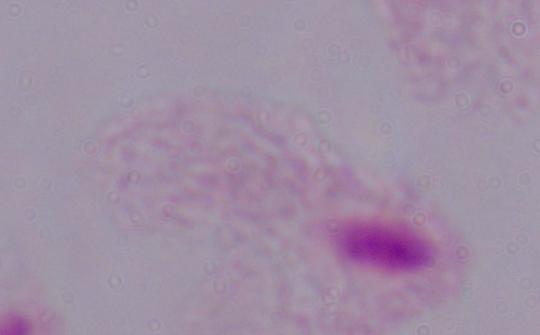

Summary:
  - Modality: photomicrograph
  - Identification: trichomonad
  - Magnification: 1000x